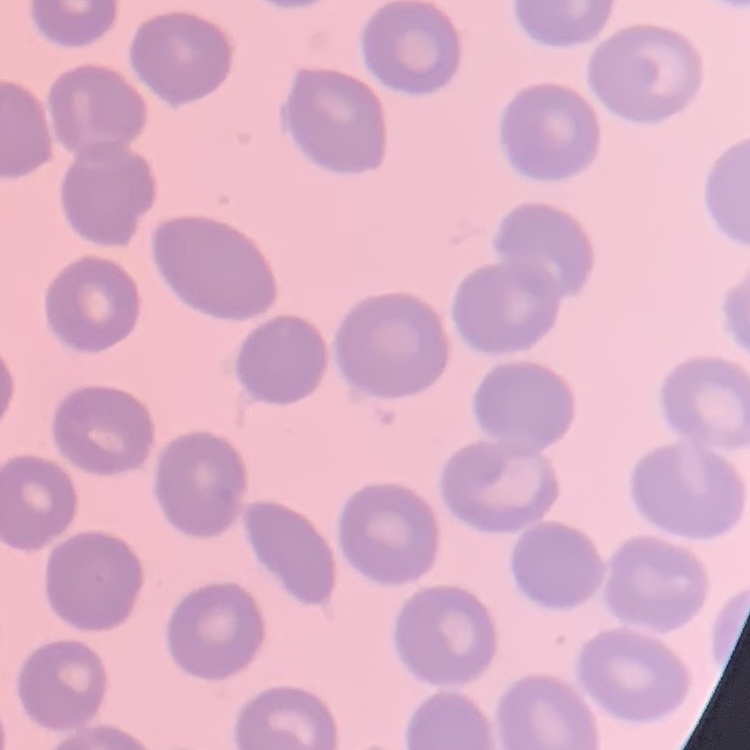
The erythrocytes exhibit no rouleaux formation. One tile cut from a larger photomicrograph. Thin peripheral smear. Stained with either Field's or Giemsa.